Assess this cell for malaria.
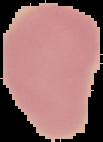
It is uninfected.

image size = 103×142 pixels
image type = segmented cell region with the area outside set to black
preparation = thin blood film